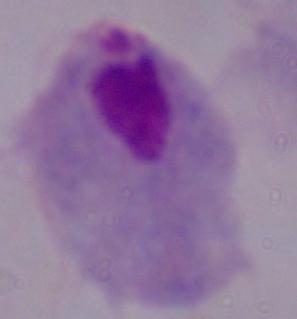
Summary:
  - Identification: trichomonad
  - Modality: micrograph
  - Magnification: 1000x